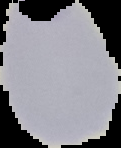

preparation = thin blood smear
image type = segmented cell region with the area outside set to black
image size = 121×148 pixels
result = malaria parasites detected